Classify this cell by malaria status.
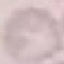

It is uninfected.

Acquired by smartphone through the microscope eyepiece. Giemsa-stained preparation. Thin blood smear. Cell patch, automatically extracted from a larger field of view and resized to 64 × 64 pixels.